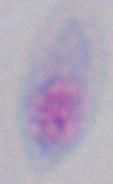
modality: micrograph
identification: Toxoplasma gondii
magnification: 1000x